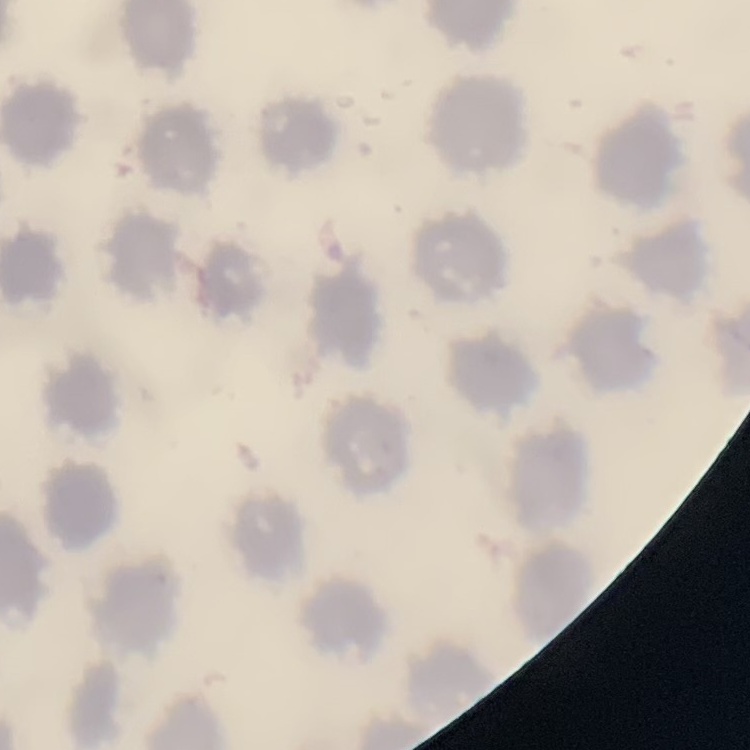

red blood cell morphology = no rouleaux formation
image type = one tile cut from a larger photomicrograph
preparation = thin peripheral smear
stain = Field's or Giemsa